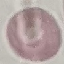

result: no malaria parasites detected
stain: Giemsa
preparation: thin blood smear
capture: smartphone through the microscope eyepiece
image_type: cell patch, automatically extracted from a larger field of view and resized to 64 × 64 pixels